State which parasite is depicted.
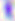
Toxoplasma gondii.

modality = photomicrograph
magnification = 400x